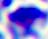

magnification = 400x
identification = white blood cell
modality = photomicrograph